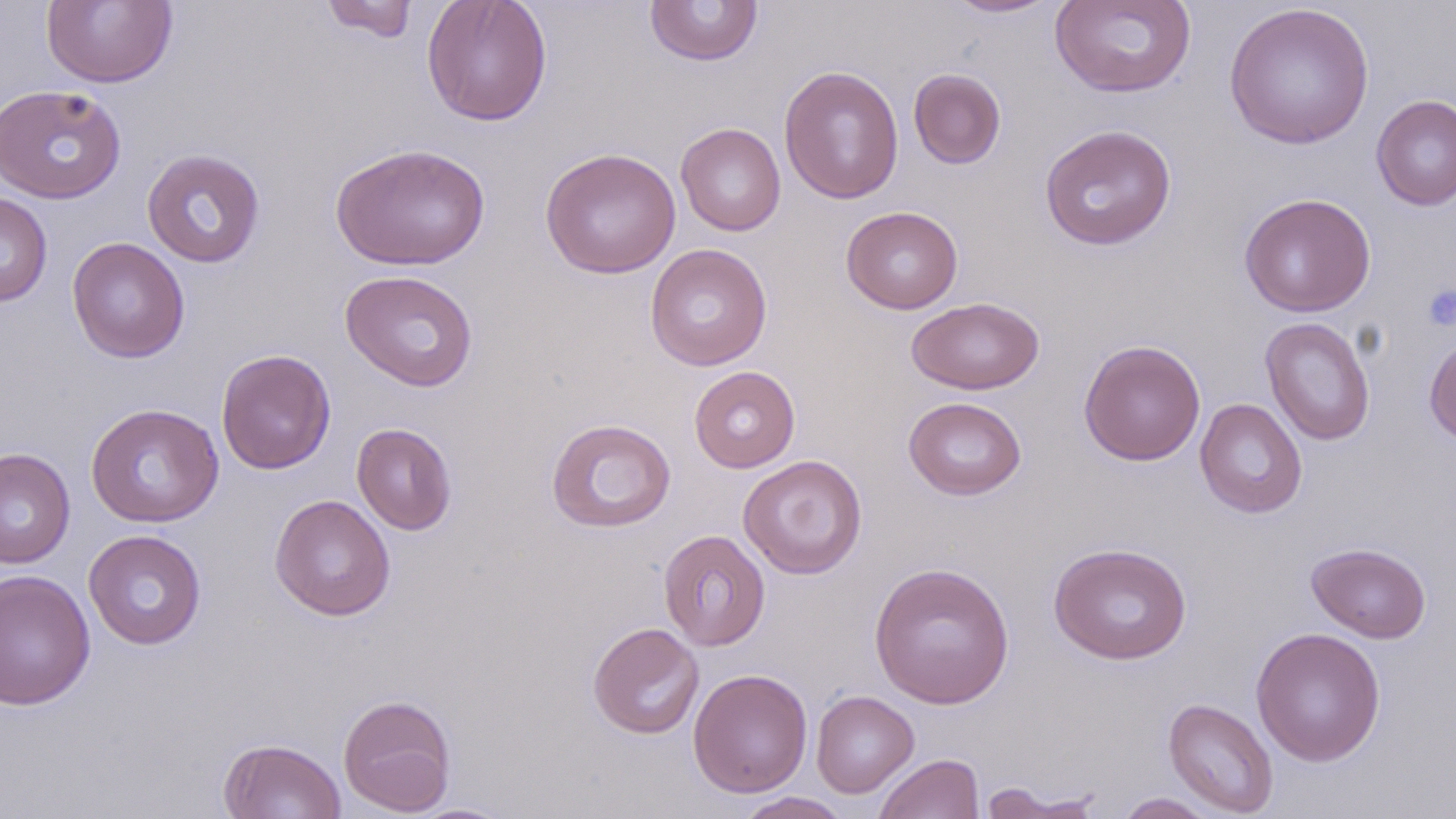

Approximate bounding boxes as named x1/y1/x2/y2 corners in pixels. Platelet locations: (x1=1422, y1=285, x2=1456, y2=331). Uninfected red blood cell locations: (x1=41, y1=0, x2=178, y2=89), (x1=319, y1=0, x2=421, y2=43), (x1=421, y1=0, x2=553, y2=127), (x1=644, y1=0, x2=763, y2=67), (x1=942, y1=0, x2=1063, y2=19), (x1=1050, y1=0, x2=1197, y2=98), (x1=1223, y1=2, x2=1375, y2=150), (x1=778, y1=65, x2=904, y2=204), (x1=908, y1=68, x2=1006, y2=169), (x1=0, y1=84, x2=126, y2=204), (x1=1371, y1=93, x2=1456, y2=211), (x1=675, y1=122, x2=786, y2=236), (x1=1039, y1=123, x2=1177, y2=251), (x1=330, y1=142, x2=491, y2=271), (x1=540, y1=147, x2=681, y2=279), (x1=142, y1=149, x2=266, y2=268), (x1=0, y1=192, x2=52, y2=307), (x1=1238, y1=193, x2=1376, y2=317), (x1=841, y1=206, x2=964, y2=315), (x1=67, y1=237, x2=190, y2=363), (x1=645, y1=243, x2=772, y2=371), (x1=339, y1=269, x2=479, y2=391), (x1=907, y1=297, x2=1045, y2=394), (x1=1260, y1=317, x2=1375, y2=446), (x1=1423, y1=334, x2=1456, y2=448), (x1=1078, y1=340, x2=1206, y2=466), (x1=216, y1=349, x2=336, y2=475), (x1=688, y1=366, x2=800, y2=473), (x1=903, y1=396, x2=1026, y2=500), (x1=1194, y1=398, x2=1307, y2=518), (x1=85, y1=403, x2=224, y2=527), (x1=546, y1=418, x2=676, y2=533), (x1=351, y1=422, x2=457, y2=535), (x1=0, y1=447, x2=75, y2=569), (x1=738, y1=455, x2=868, y2=579), (x1=270, y1=494, x2=396, y2=620), (x1=658, y1=529, x2=771, y2=651), (x1=83, y1=530, x2=207, y2=650), (x1=1048, y1=541, x2=1192, y2=664), (x1=1306, y1=542, x2=1431, y2=643), (x1=868, y1=562, x2=1015, y2=709), (x1=1, y1=568, x2=96, y2=710), (x1=587, y1=622, x2=704, y2=739), (x1=1250, y1=626, x2=1386, y2=766), (x1=688, y1=668, x2=813, y2=798), (x1=810, y1=690, x2=919, y2=798), (x1=338, y1=693, x2=457, y2=816), (x1=1163, y1=696, x2=1279, y2=818), (x1=218, y1=738, x2=347, y2=819), (x1=873, y1=753, x2=985, y2=819), (x1=977, y1=783, x2=1105, y2=819), (x1=732, y1=792, x2=854, y2=819), (x1=1113, y1=792, x2=1220, y2=818), (x1=407, y1=802, x2=515, y2=818). Slide-level diagnosis: negative for blood parasites. Single field of view. Thin blood smear. May-Grünwald-Giemsa-stained preparation. Captured at 1000x magnification. Light microscopy. Image is 1456×819 pixels.